Identify the parasite.
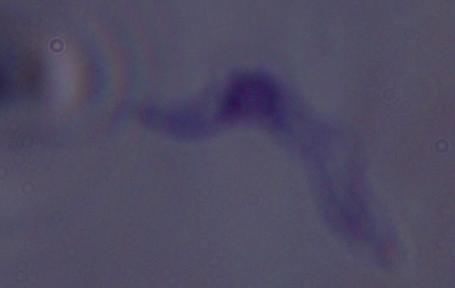
A trypanosome.

{
  "modality": "micrograph",
  "magnification": "1000x"
}